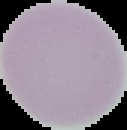

Summary:
  - Result: negative for malaria parasites
  - Image type: cell region segmented out of the field of view; surrounding area masked to black
  - Image size: 127×130 pixels
  - Preparation: thin blood film